Assess the morphology of the erythrocytes.
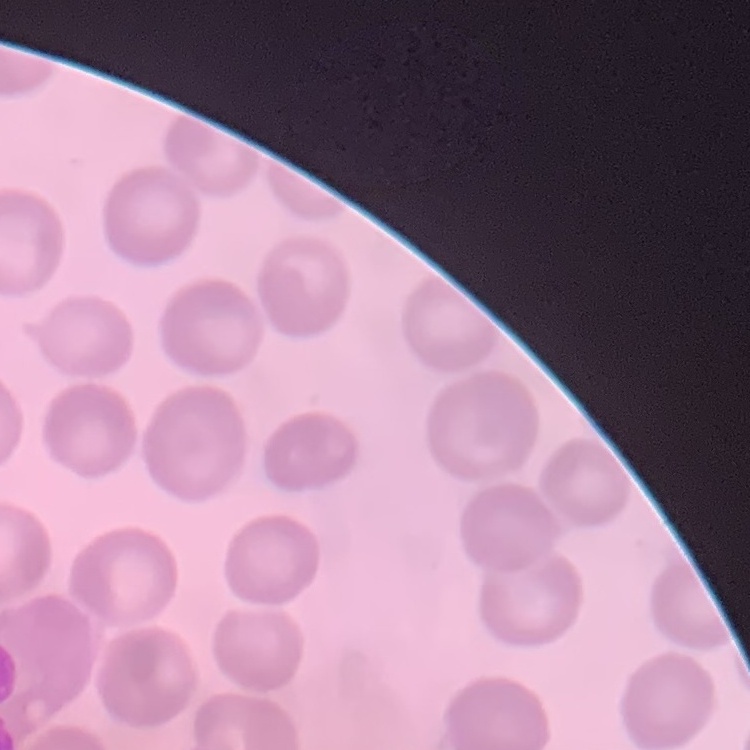

No rouleaux formation.

Field's or Giemsa stain. Square crop of a larger photomicrograph. Thin blood smear.